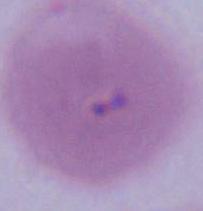 An erythrocyte is seen. Micrograph. 1000x magnification.